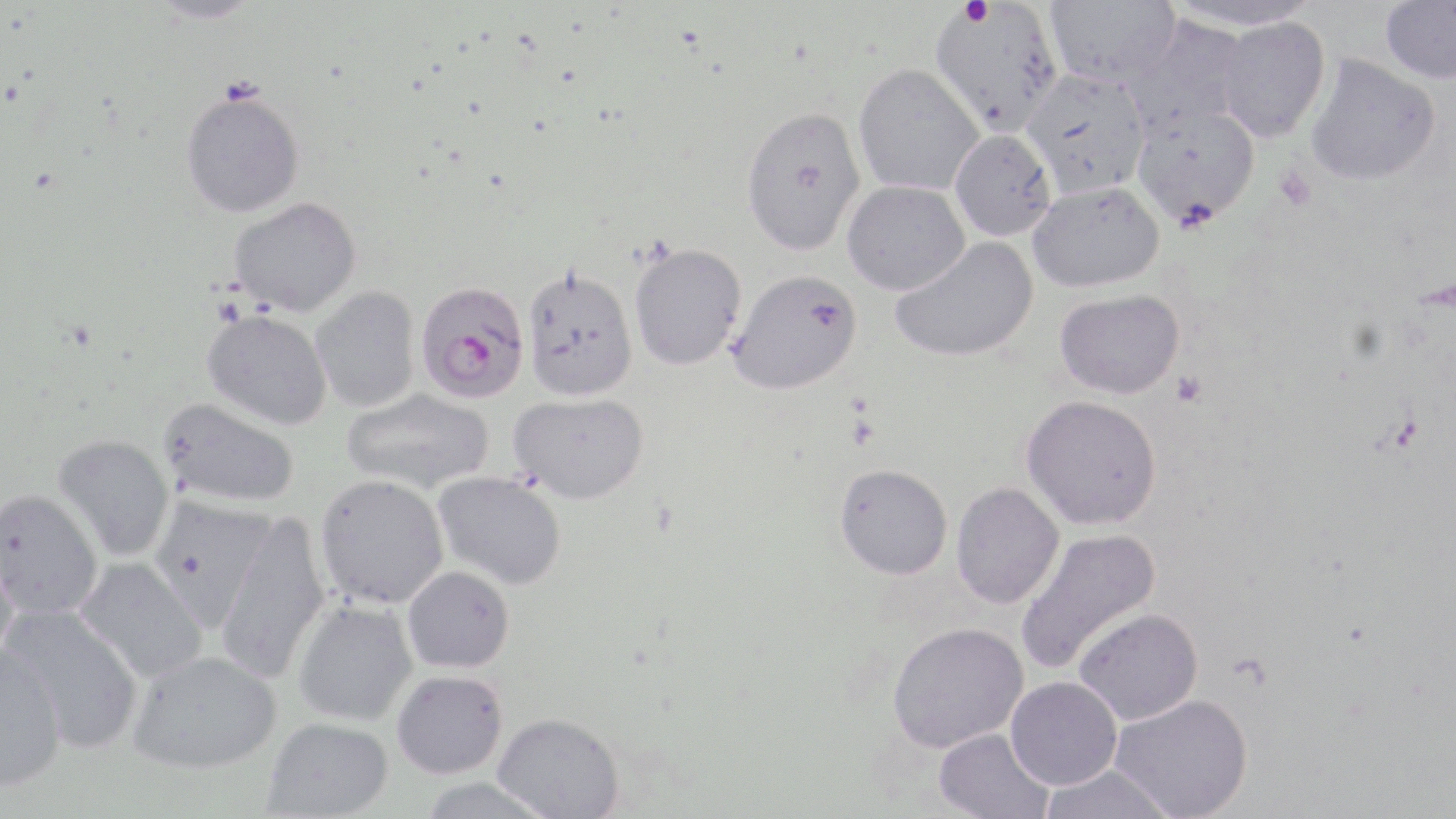
slide_level_diagnosis: Plasmodium falciparum
magnification: 1000x
modality: light microscopy
plasmodium_falciparum_infected_red_blood_cell_locations: 'approximate bounding boxes as [x1, y1, x2, y2] in pixels: [415, 282, 531, 405]'
preparation: thin blood film
image_size: 1456×819 pixels
field_of_view: one of a larger specimen
stain: May-Grünwald-Giemsa
platelet_locations: 'approximate bounding boxes as [x1, y1, x2, y2] in pixels: [961, 1, 994, 28], [1170, 370, 1207, 407]'
uninfected_red_blood_cell_locations: 'approximate bounding boxes as [x1, y1, x2, y2] in pixels: [1044, 0, 1180, 91], [1380, 0, 1456, 86], [148, 1, 263, 27], [1166, 1, 1325, 30], [929, 3, 1063, 138], [1123, 18, 1248, 138], [1213, 18, 1330, 144], [1305, 55, 1441, 188], [852, 66, 984, 197], [1021, 70, 1152, 200], [180, 95, 305, 220], [1132, 106, 1260, 229], [740, 109, 867, 259], [949, 130, 1056, 242], [842, 181, 970, 297], [1028, 182, 1165, 293], [229, 199, 361, 319], [890, 236, 1040, 363], [629, 243, 747, 372], [522, 269, 638, 404], [726, 270, 864, 399], [310, 286, 421, 412], [1055, 289, 1186, 400], [201, 311, 332, 431], [342, 388, 495, 494], [508, 393, 648, 506], [1021, 395, 1162, 530], [158, 398, 299, 508], [52, 434, 175, 562], [834, 464, 953, 580], [432, 471, 567, 590], [314, 475, 449, 610], [951, 482, 1064, 609], [0, 489, 103, 619], [148, 494, 277, 631], [215, 513, 331, 683], [1016, 527, 1161, 674], [0, 539, 20, 670], [72, 556, 208, 683], [403, 567, 514, 674], [292, 599, 418, 727], [2, 603, 143, 753], [1074, 608, 1203, 725], [887, 622, 1029, 752], [0, 646, 67, 791], [127, 650, 282, 776], [392, 671, 508, 780], [1006, 676, 1122, 789], [1110, 694, 1253, 819], [492, 713, 625, 818], [262, 718, 393, 819], [934, 728, 1055, 818], [1038, 764, 1177, 819], [415, 777, 557, 819]'